Give the extent of all Plasmodium falciparum-infected red blood cells.
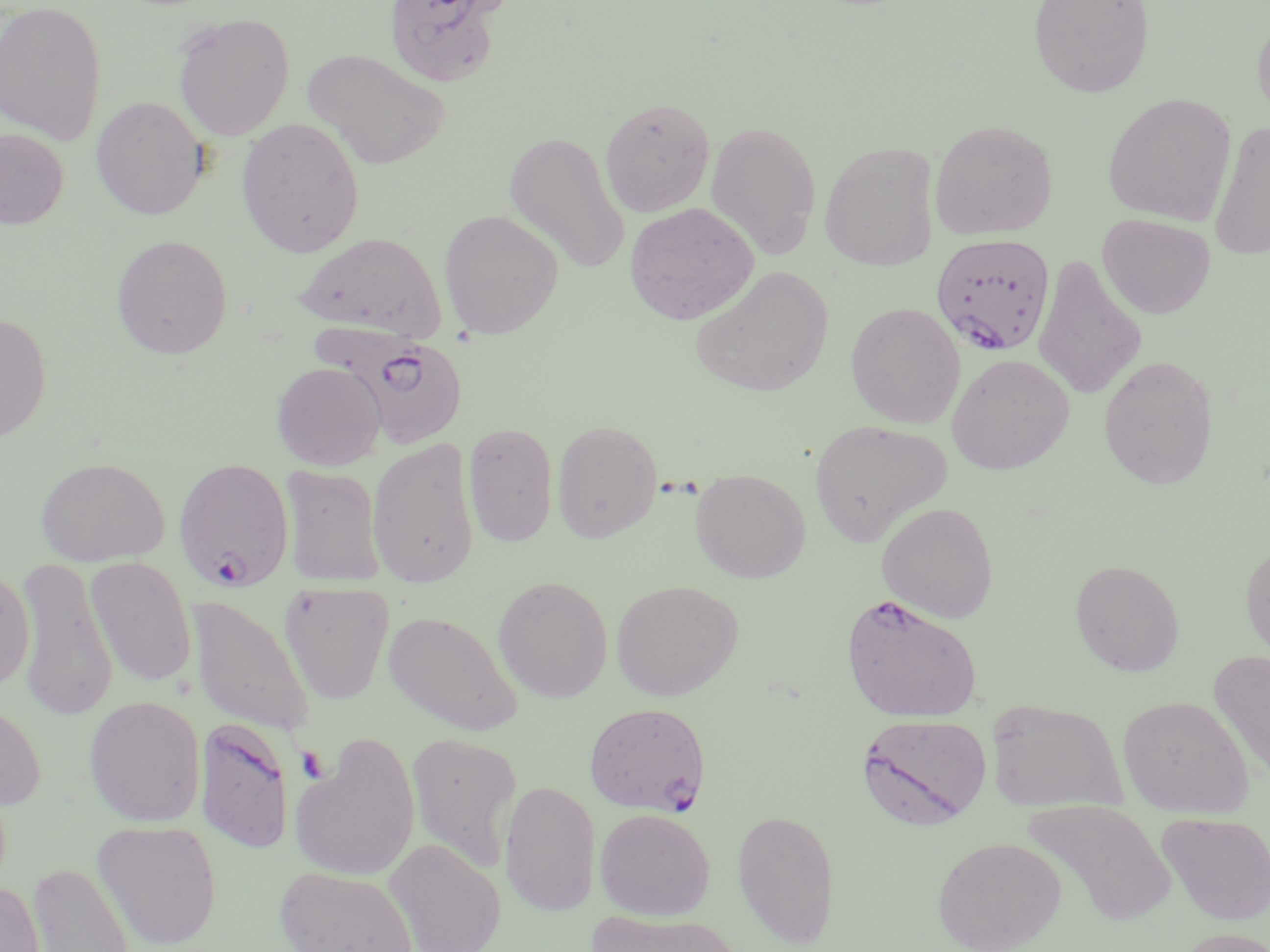
Approximate bounding boxes as named x1/y1/x2/y2 corners in pixels.
Plasmodium falciparum-infected red blood cells: (x1=931, y1=234, x2=1056, y2=355), (x1=336, y1=329, x2=472, y2=451), (x1=173, y1=457, x2=295, y2=592), (x1=840, y1=593, x2=984, y2=723), (x1=584, y1=702, x2=710, y2=816), (x1=855, y1=713, x2=991, y2=829), (x1=195, y1=717, x2=295, y2=854).

slide-level diagnosis = Plasmodium falciparum
preparation = thin blood smear
image size = 1270×952 pixels
modality = light microscopy
magnification = 1000x
field of view = one of a larger specimen
stain = May-Grünwald-Giemsa
platelet locations = approximate bounding boxes as named x1/y1/x2/y2 corners in pixels: (x1=297, y1=745, x2=330, y2=783)
uninfected red blood cell locations = approximate bounding boxes as named x1/y1/x2/y2 corners in pixels: (x1=384, y1=0, x2=509, y2=87), (x1=1028, y1=0, x2=1155, y2=98), (x1=0, y1=1, x2=108, y2=144), (x1=1252, y1=8, x2=1270, y2=125), (x1=172, y1=12, x2=295, y2=141), (x1=301, y1=47, x2=451, y2=170), (x1=1102, y1=93, x2=1237, y2=225), (x1=91, y1=96, x2=209, y2=220), (x1=600, y1=97, x2=715, y2=217), (x1=236, y1=117, x2=365, y2=258), (x1=705, y1=119, x2=823, y2=259), (x1=929, y1=119, x2=1059, y2=239), (x1=1208, y1=120, x2=1270, y2=262), (x1=0, y1=128, x2=69, y2=229), (x1=504, y1=129, x2=630, y2=276), (x1=819, y1=140, x2=940, y2=271), (x1=623, y1=202, x2=759, y2=325), (x1=439, y1=209, x2=564, y2=339), (x1=1098, y1=213, x2=1216, y2=319), (x1=295, y1=231, x2=446, y2=340), (x1=110, y1=234, x2=233, y2=359), (x1=1033, y1=254, x2=1146, y2=402), (x1=690, y1=266, x2=834, y2=397), (x1=845, y1=302, x2=965, y2=428), (x1=0, y1=312, x2=52, y2=442), (x1=947, y1=353, x2=1075, y2=474), (x1=1098, y1=354, x2=1219, y2=490), (x1=271, y1=361, x2=387, y2=470), (x1=552, y1=418, x2=663, y2=542), (x1=809, y1=418, x2=952, y2=546), (x1=464, y1=422, x2=559, y2=548), (x1=367, y1=438, x2=480, y2=589), (x1=34, y1=455, x2=170, y2=567), (x1=279, y1=465, x2=386, y2=587), (x1=690, y1=469, x2=811, y2=582), (x1=876, y1=502, x2=999, y2=623), (x1=1240, y1=538, x2=1270, y2=666), (x1=85, y1=557, x2=197, y2=687), (x1=14, y1=558, x2=118, y2=721), (x1=1070, y1=559, x2=1185, y2=676), (x1=0, y1=565, x2=35, y2=693), (x1=493, y1=576, x2=613, y2=702), (x1=610, y1=580, x2=743, y2=701), (x1=279, y1=582, x2=394, y2=704), (x1=186, y1=595, x2=315, y2=735), (x1=383, y1=610, x2=522, y2=736), (x1=1208, y1=650, x2=1270, y2=785), (x1=84, y1=695, x2=206, y2=827), (x1=0, y1=696, x2=46, y2=810), (x1=1117, y1=696, x2=1253, y2=818), (x1=985, y1=698, x2=1126, y2=812), (x1=406, y1=731, x2=522, y2=873), (x1=290, y1=735, x2=420, y2=883), (x1=500, y1=780, x2=601, y2=917), (x1=1022, y1=799, x2=1176, y2=928), (x1=732, y1=807, x2=839, y2=948), (x1=595, y1=808, x2=715, y2=920), (x1=1157, y1=812, x2=1270, y2=925), (x1=91, y1=819, x2=223, y2=950), (x1=932, y1=836, x2=1066, y2=952), (x1=384, y1=837, x2=506, y2=952), (x1=27, y1=861, x2=136, y2=952), (x1=274, y1=866, x2=417, y2=952), (x1=0, y1=879, x2=45, y2=951), (x1=587, y1=911, x2=744, y2=952), (x1=1173, y1=927, x2=1270, y2=952)